State the blood parasite species.
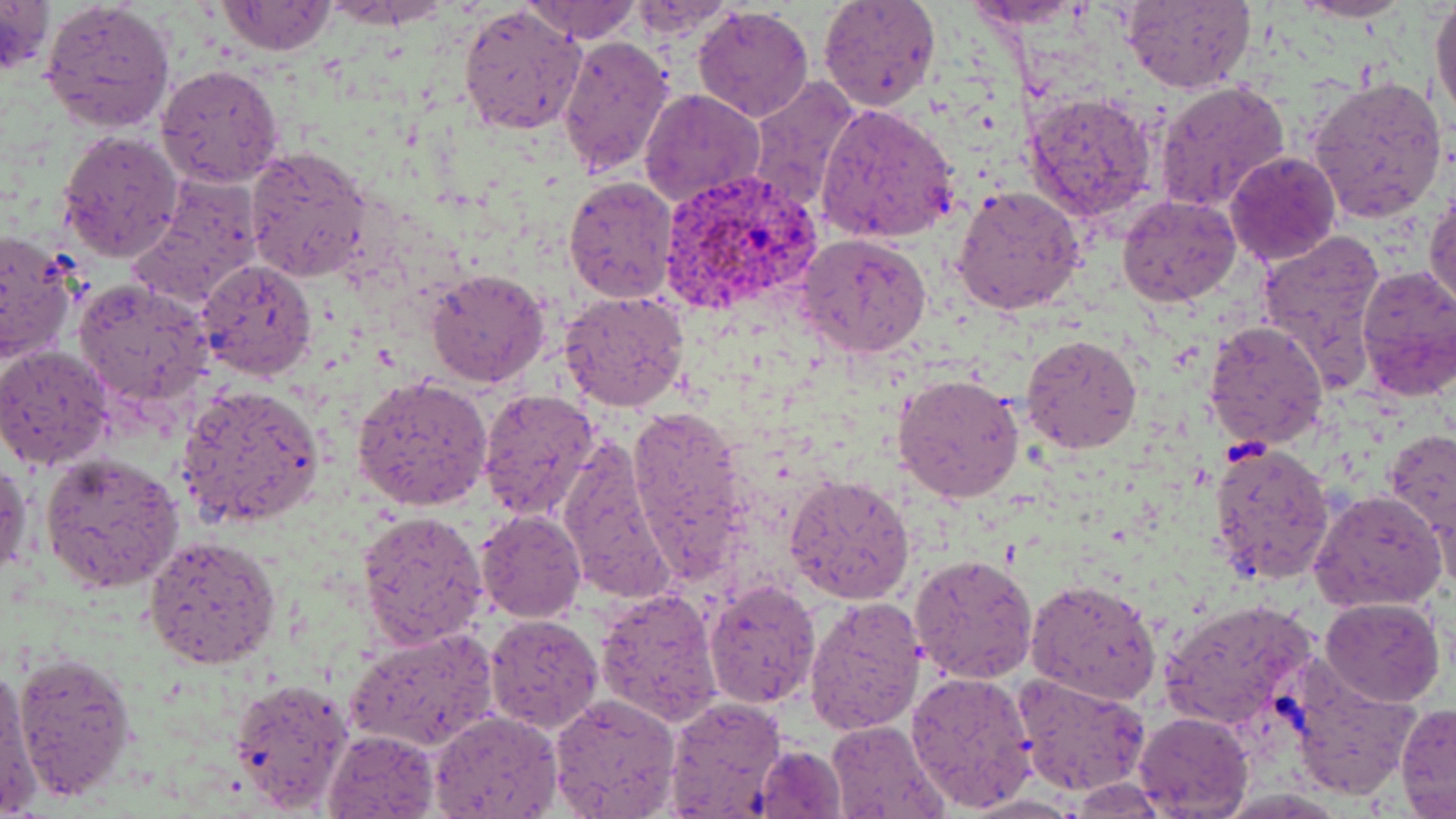

Plasmodium vivax.

field of view = one of a larger specimen
uninfected red blood cell locations = approximate bounding boxes as (x1,y1)-(x2,y2) corner pairs in pixels: (0,0)-(54,77), (524,0)-(640,42), (817,0)-(942,111), (1296,0)-(1408,23), (1431,0)-(1455,125), (39,1)-(176,133), (215,1)-(337,56), (1120,1)-(1255,92), (963,2)-(1086,29), (458,4)-(585,137), (620,4)-(740,39), (692,5)-(814,121), (555,35)-(673,180), (156,63)-(286,189), (1306,74)-(1448,224), (747,78)-(860,215), (1153,81)-(1291,212), (640,89)-(764,207), (1024,91)-(1158,219), (816,103)-(960,244), (57,129)-(184,262), (246,147)-(373,281), (1224,149)-(1342,265), (129,174)-(265,307), (562,174)-(678,305), (1426,179)-(1456,314), (953,185)-(1086,317), (1117,195)-(1240,307), (0,229)-(81,364), (1256,231)-(1388,371), (796,234)-(932,358), (198,259)-(319,380), (1354,265)-(1456,397), (424,268)-(549,389), (74,279)-(214,406), (559,290)-(691,414), (1204,320)-(1327,448), (1020,332)-(1143,455), (0,345)-(115,470), (893,371)-(1024,505), (352,376)-(494,510), (173,382)-(326,528), (477,389)-(601,522), (626,403)-(751,581), (1382,432)-(1455,533), (555,433)-(678,606), (1209,443)-(1335,584), (40,452)-(185,593), (0,458)-(31,581), (785,474)-(915,605), (1310,490)-(1447,613), (1426,492)-(1454,597), (475,509)-(587,623), (358,510)-(490,648), (144,534)-(281,667), (910,553)-(1039,682), (1026,576)-(1161,706), (704,579)-(821,708), (595,587)-(723,726), (804,596)-(927,737), (1320,597)-(1444,706), (1160,599)-(1316,732), (484,613)-(603,734), (345,627)-(499,750), (12,650)-(140,800), (1284,656)-(1420,800), (0,665)-(40,816), (904,670)-(1037,813), (1011,674)-(1150,797), (226,678)-(354,817), (548,694)-(680,818), (663,695)-(786,818), (1395,702)-(1456,816), (429,710)-(562,818), (1134,710)-(1253,816), (826,719)-(949,818), (323,728)-(439,818), (753,742)-(850,819), (1070,777)-(1170,817)
stain = May-Grünwald-Giemsa
preparation = thin blood film
magnification = 1000x
Plasmodium vivax-infected red blood cell locations = approximate bounding boxes as (x1,y1)-(x2,y2) corner pairs in pixels: (657,169)-(821,318)
image size = 1456×819 pixels
modality = light microscopy